Assess the morphology of the erythrocytes.
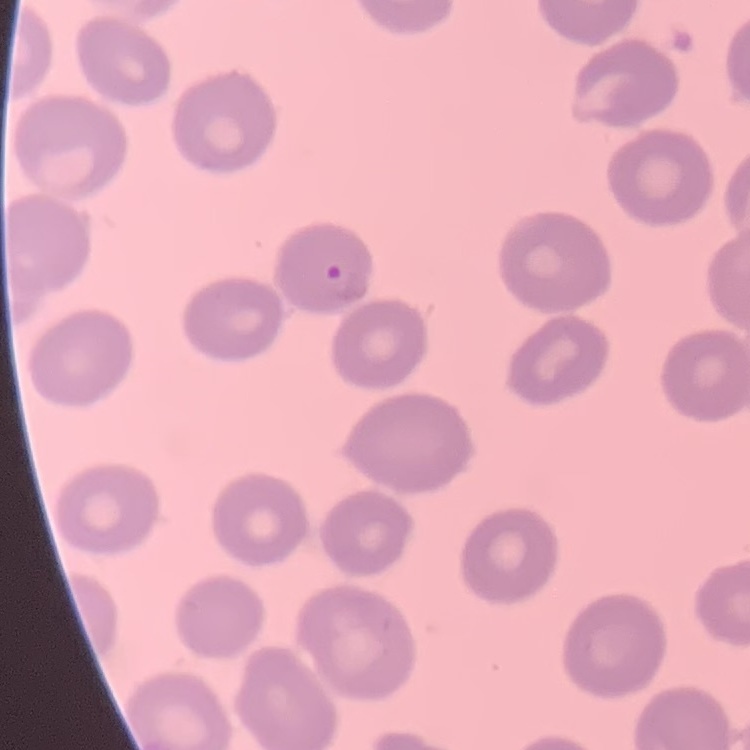

No rouleaux formation.

Thin blood smear. One tile cut from a larger photomicrograph. Stained with either Field's or Giemsa.